Comment on the morphology of the erythrocytes.
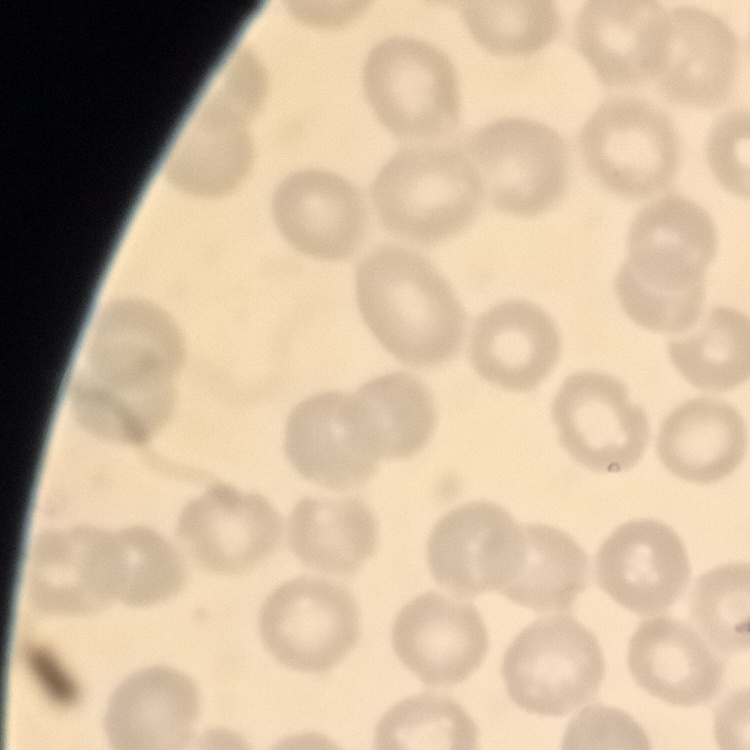

No rouleaux formation.

Summary:
  - Preparation: thin blood smear
  - Stain: Field's or Giemsa
  - Image type: one tile cut from a larger photomicrograph